State which cell type is depicted.
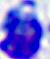
This is a leukocyte.

400x magnification. Photomicrograph.